Report the malaria status of this cell.
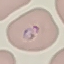

It is parasitized.

Acquired by smartphone through the microscope eyepiece. Automatically extracted cell patch, resized to 64 × 64 pixels. Thin blood smear. Giemsa stain.